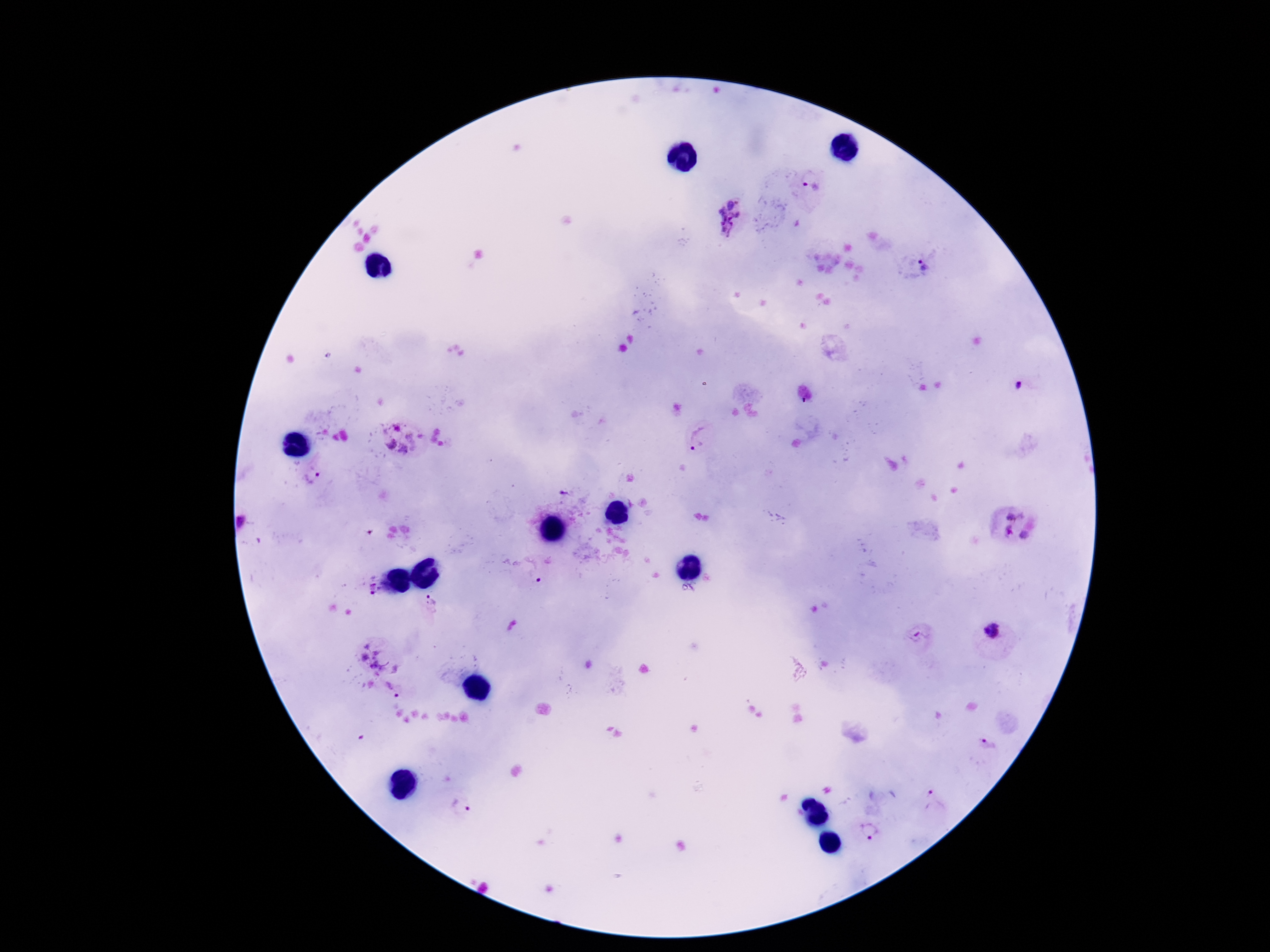
Approximate centers as (x, y) in pixels. Plasmodium parasite locations: (813, 185), (727, 217), (922, 266), (698, 437), (403, 438), (312, 478), (567, 493), (1015, 511), (242, 522), (1007, 531), (1023, 535), (539, 577), (373, 589), (430, 599), (992, 631), (920, 634), (373, 657), (392, 688), (933, 802), (462, 805), (871, 833). Giemsa stain. Photographed through the microscope eyepiece with a smartphone camera. Image is 1270×952 pixels. Patient malaria status: positive. One field from this slide. Thick blood film. 100x magnification.